Identify the cell.
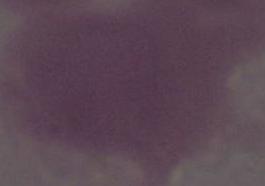

An erythrocyte.

Summary:
  - Modality: micrograph
  - Magnification: 1000x